Assess this cell for malaria.
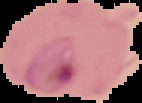
Parasitized.

image type = cell region segmented out of the field of view; surrounding area masked to black
preparation = thin blood smear
image size = 142×103 pixels